Classify this cell by malaria status.
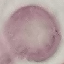

Uninfected.

Summary:
  - Capture: smartphone camera at the microscope eyepiece
  - Image type: cell patch, automatically extracted from a larger field of view and resized to 64 × 64 pixels
  - Preparation: thin blood film
  - Stain: Giemsa